Give the extent of all uninfected red blood cells.
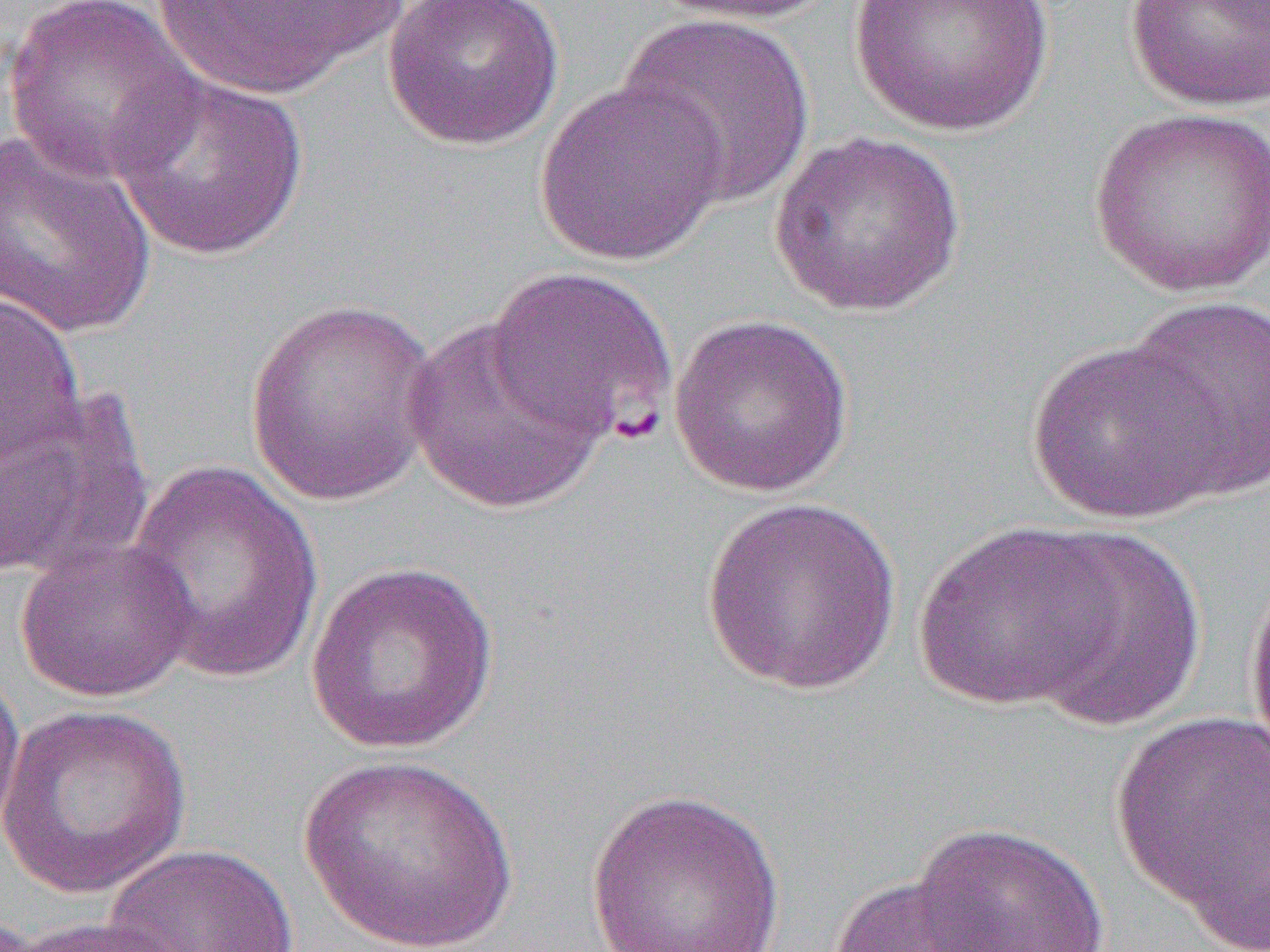

Approximate bounding boxes as (x1,y1)-(x2,y2) corner pairs in pixels.
Uninfected red blood cells: (3,0)-(206,187), (148,0)-(410,99), (382,0)-(565,151), (651,0)-(837,26), (848,0)-(1054,138), (1123,0)-(1270,113), (616,12)-(817,208), (107,69)-(311,261), (534,79)-(728,266), (1088,106)-(1270,297), (0,131)-(158,340), (768,131)-(967,317), (485,265)-(678,447), (0,292)-(88,465), (1122,296)-(1270,500), (243,299)-(442,506), (667,312)-(856,498), (402,314)-(612,515), (1025,339)-(1230,524), (0,388)-(153,584), (124,460)-(324,686), (699,496)-(904,696), (913,520)-(1126,712), (1023,526)-(1210,731), (15,535)-(199,703), (1243,555)-(1270,768), (304,561)-(502,754), (0,661)-(25,838), (0,703)-(193,898), (1110,709)-(1270,932), (297,753)-(518,952), (584,787)-(787,952), (1177,790)-(1269,952), (906,820)-(1113,952), (102,843)-(301,952), (827,872)-(1004,952), (13,916)-(192,952).

slide-level diagnosis = Plasmodium falciparum
modality = optical microscopy
preparation = thin blood film
field of view = single
image size = 1270×952 pixels
magnification = 1000x